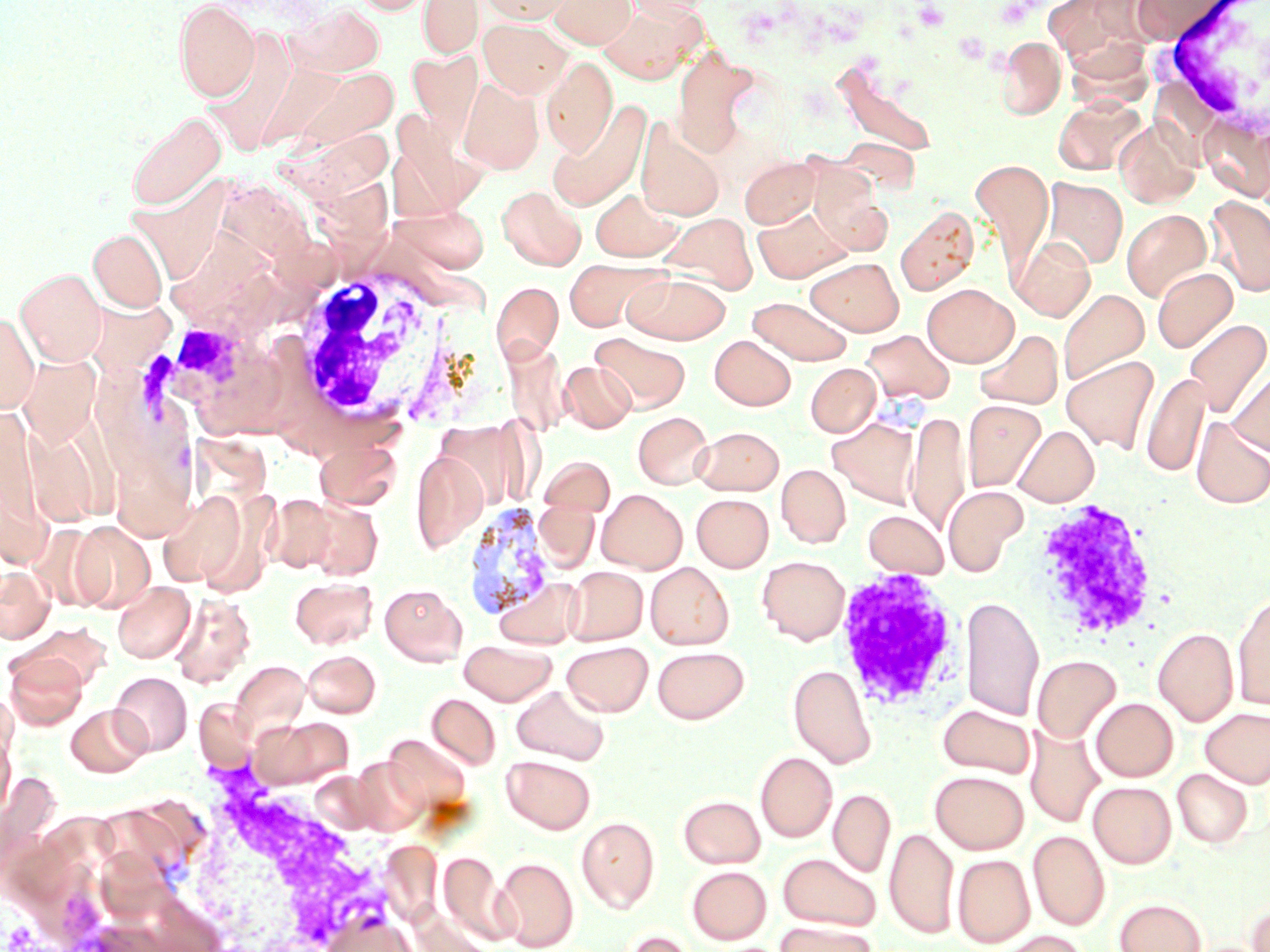
slide-level diagnosis = Plasmodium vivax
magnification = 1000x
field of view = single
stain = May-Grünwald-Giemsa
platelet locations = approximate bounding boxes as named x1/y1/x2/y2 corners in pixels: (x1=912, y1=2, x2=950, y2=31)
Plasmodium vivax-infected red blood cell locations = approximate bounding boxes as named x1/y1/x2/y2 corners in pixels: (x1=463, y1=501, x2=558, y2=626)
white blood cell locations = approximate bounding boxes as named x1/y1/x2/y2 corners in pixels: (x1=1147, y1=0, x2=1270, y2=146), (x1=283, y1=266, x2=444, y2=437), (x1=131, y1=317, x2=262, y2=408), (x1=947, y1=490, x2=1029, y2=569), (x1=1029, y1=499, x2=1161, y2=642), (x1=833, y1=567, x2=971, y2=719), (x1=167, y1=766, x2=405, y2=952)
modality = light microscopy
uninfected red blood cell locations = approximate bounding boxes as named x1/y1/x2/y2 corners in pixels: (x1=174, y1=0, x2=260, y2=102), (x1=352, y1=0, x2=435, y2=16), (x1=418, y1=0, x2=483, y2=58), (x1=477, y1=0, x2=577, y2=25), (x1=547, y1=0, x2=638, y2=49), (x1=624, y1=0, x2=715, y2=20), (x1=1130, y1=0, x2=1230, y2=43), (x1=284, y1=3, x2=385, y2=78), (x1=596, y1=3, x2=703, y2=83), (x1=478, y1=19, x2=572, y2=99), (x1=201, y1=30, x2=300, y2=155), (x1=995, y1=36, x2=1066, y2=119), (x1=673, y1=49, x2=757, y2=157), (x1=406, y1=50, x2=482, y2=141), (x1=542, y1=55, x2=617, y2=157), (x1=830, y1=56, x2=939, y2=161), (x1=282, y1=65, x2=399, y2=153), (x1=456, y1=77, x2=544, y2=175), (x1=1053, y1=95, x2=1145, y2=175), (x1=546, y1=99, x2=651, y2=212), (x1=126, y1=111, x2=226, y2=210), (x1=636, y1=118, x2=725, y2=221), (x1=1114, y1=119, x2=1200, y2=208), (x1=270, y1=125, x2=400, y2=207), (x1=837, y1=136, x2=919, y2=195), (x1=739, y1=156, x2=821, y2=228), (x1=970, y1=159, x2=1054, y2=270), (x1=811, y1=171, x2=890, y2=252), (x1=120, y1=174, x2=236, y2=294), (x1=1041, y1=178, x2=1128, y2=270), (x1=497, y1=185, x2=585, y2=270), (x1=590, y1=189, x2=683, y2=261), (x1=1206, y1=194, x2=1270, y2=298), (x1=395, y1=204, x2=490, y2=272), (x1=752, y1=206, x2=851, y2=283), (x1=895, y1=206, x2=978, y2=296), (x1=1121, y1=208, x2=1212, y2=301), (x1=659, y1=213, x2=758, y2=294), (x1=170, y1=223, x2=281, y2=320), (x1=89, y1=228, x2=167, y2=312), (x1=1011, y1=236, x2=1095, y2=320), (x1=806, y1=257, x2=904, y2=336), (x1=562, y1=260, x2=667, y2=332), (x1=16, y1=267, x2=106, y2=366), (x1=1153, y1=267, x2=1237, y2=352), (x1=623, y1=272, x2=731, y2=344), (x1=491, y1=281, x2=563, y2=364), (x1=922, y1=284, x2=1018, y2=366), (x1=1058, y1=288, x2=1149, y2=385), (x1=748, y1=296, x2=852, y2=365), (x1=83, y1=297, x2=179, y2=386), (x1=1, y1=313, x2=38, y2=411), (x1=1183, y1=317, x2=1270, y2=418), (x1=976, y1=329, x2=1063, y2=409), (x1=862, y1=330, x2=953, y2=405), (x1=591, y1=333, x2=690, y2=413), (x1=709, y1=335, x2=796, y2=410), (x1=502, y1=341, x2=570, y2=437), (x1=17, y1=354, x2=101, y2=449), (x1=1061, y1=355, x2=1159, y2=453), (x1=560, y1=360, x2=635, y2=433), (x1=805, y1=363, x2=881, y2=437), (x1=1228, y1=365, x2=1270, y2=456), (x1=1141, y1=372, x2=1210, y2=477), (x1=963, y1=399, x2=1047, y2=491), (x1=633, y1=411, x2=714, y2=489), (x1=907, y1=411, x2=970, y2=534), (x1=827, y1=415, x2=922, y2=508), (x1=1191, y1=417, x2=1270, y2=508), (x1=25, y1=424, x2=102, y2=530), (x1=1013, y1=425, x2=1099, y2=506), (x1=693, y1=426, x2=784, y2=495), (x1=314, y1=439, x2=402, y2=511), (x1=410, y1=449, x2=488, y2=554), (x1=538, y1=455, x2=615, y2=516), (x1=776, y1=464, x2=850, y2=548), (x1=944, y1=485, x2=1026, y2=573), (x1=597, y1=489, x2=687, y2=573), (x1=158, y1=491, x2=248, y2=588), (x1=264, y1=493, x2=341, y2=573), (x1=692, y1=494, x2=773, y2=571), (x1=304, y1=499, x2=382, y2=579), (x1=863, y1=510, x2=949, y2=578), (x1=68, y1=520, x2=155, y2=612), (x1=757, y1=555, x2=850, y2=644), (x1=646, y1=562, x2=733, y2=649), (x1=0, y1=564, x2=54, y2=643), (x1=564, y1=566, x2=648, y2=645), (x1=289, y1=576, x2=378, y2=649), (x1=112, y1=580, x2=196, y2=663), (x1=379, y1=583, x2=467, y2=665), (x1=169, y1=592, x2=256, y2=688), (x1=1232, y1=592, x2=1270, y2=710), (x1=961, y1=595, x2=1043, y2=722), (x1=16, y1=623, x2=110, y2=693), (x1=1153, y1=627, x2=1238, y2=725), (x1=458, y1=639, x2=557, y2=705), (x1=562, y1=641, x2=653, y2=716), (x1=652, y1=646, x2=750, y2=723), (x1=302, y1=649, x2=381, y2=717), (x1=4, y1=652, x2=88, y2=730), (x1=1032, y1=655, x2=1120, y2=743), (x1=230, y1=660, x2=310, y2=738), (x1=788, y1=664, x2=876, y2=768), (x1=109, y1=671, x2=192, y2=756), (x1=511, y1=685, x2=609, y2=766), (x1=427, y1=693, x2=500, y2=769), (x1=1091, y1=698, x2=1177, y2=781), (x1=67, y1=704, x2=150, y2=776), (x1=938, y1=704, x2=1036, y2=778), (x1=1200, y1=707, x2=1270, y2=787), (x1=253, y1=717, x2=354, y2=788), (x1=1187, y1=718, x2=1263, y2=839), (x1=0, y1=727, x2=15, y2=822), (x1=1025, y1=727, x2=1104, y2=828), (x1=383, y1=735, x2=470, y2=814), (x1=755, y1=752, x2=837, y2=842), (x1=501, y1=755, x2=595, y2=834), (x1=348, y1=759, x2=427, y2=834), (x1=1172, y1=769, x2=1253, y2=847), (x1=930, y1=770, x2=1029, y2=854), (x1=1088, y1=781, x2=1176, y2=867), (x1=828, y1=789, x2=895, y2=876), (x1=678, y1=795, x2=765, y2=868), (x1=576, y1=816, x2=659, y2=912), (x1=884, y1=828, x2=959, y2=939), (x1=1028, y1=830, x2=1109, y2=930), (x1=439, y1=851, x2=511, y2=943), (x1=778, y1=852, x2=882, y2=931), (x1=953, y1=854, x2=1034, y2=947), (x1=494, y1=856, x2=578, y2=951), (x1=687, y1=865, x2=771, y2=944), (x1=1114, y1=899, x2=1205, y2=952), (x1=1246, y1=903, x2=1270, y2=952), (x1=413, y1=911, x2=499, y2=952), (x1=323, y1=913, x2=422, y2=952), (x1=774, y1=921, x2=877, y2=952), (x1=618, y1=929, x2=698, y2=952), (x1=1000, y1=931, x2=1090, y2=952)
preparation = thin blood film
image size = 1270×952 pixels